Report the malaria status of this cell.
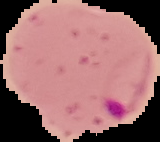

Parasitized.

Summary:
  - Preparation: thin blood film
  - Image size: 160×142 pixels
  - Image type: cell region segmented out of the field of view; surrounding area masked to black